State which parasite is depicted.
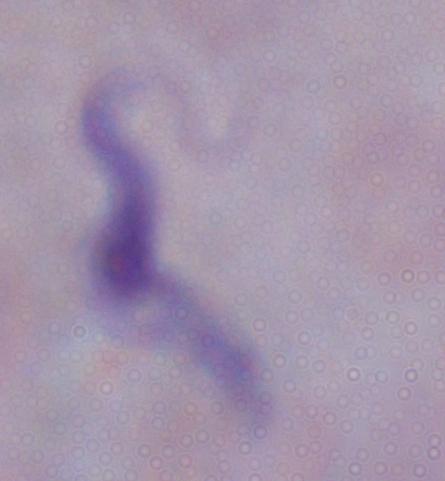

A trypanosome.

Photomicrograph. Captured at 1000x magnification.